Describe the morphology of the erythrocytes.
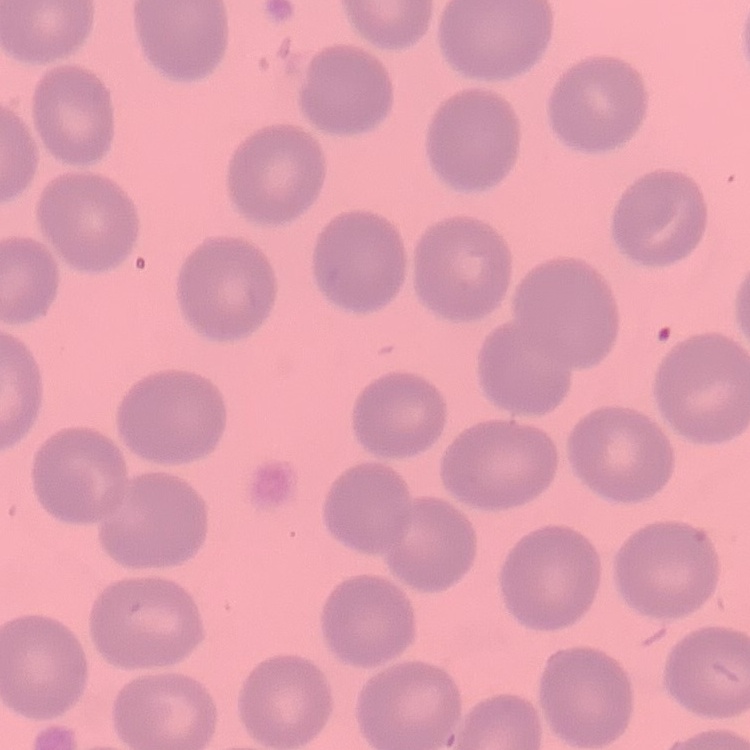

They show no rouleaux formation.

image type = square crop of a larger photomicrograph
preparation = thin peripheral smear
stain = Field's or Giemsa